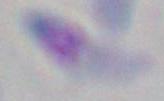

1000x magnification. Micrograph. Toxoplasma gondii is seen.